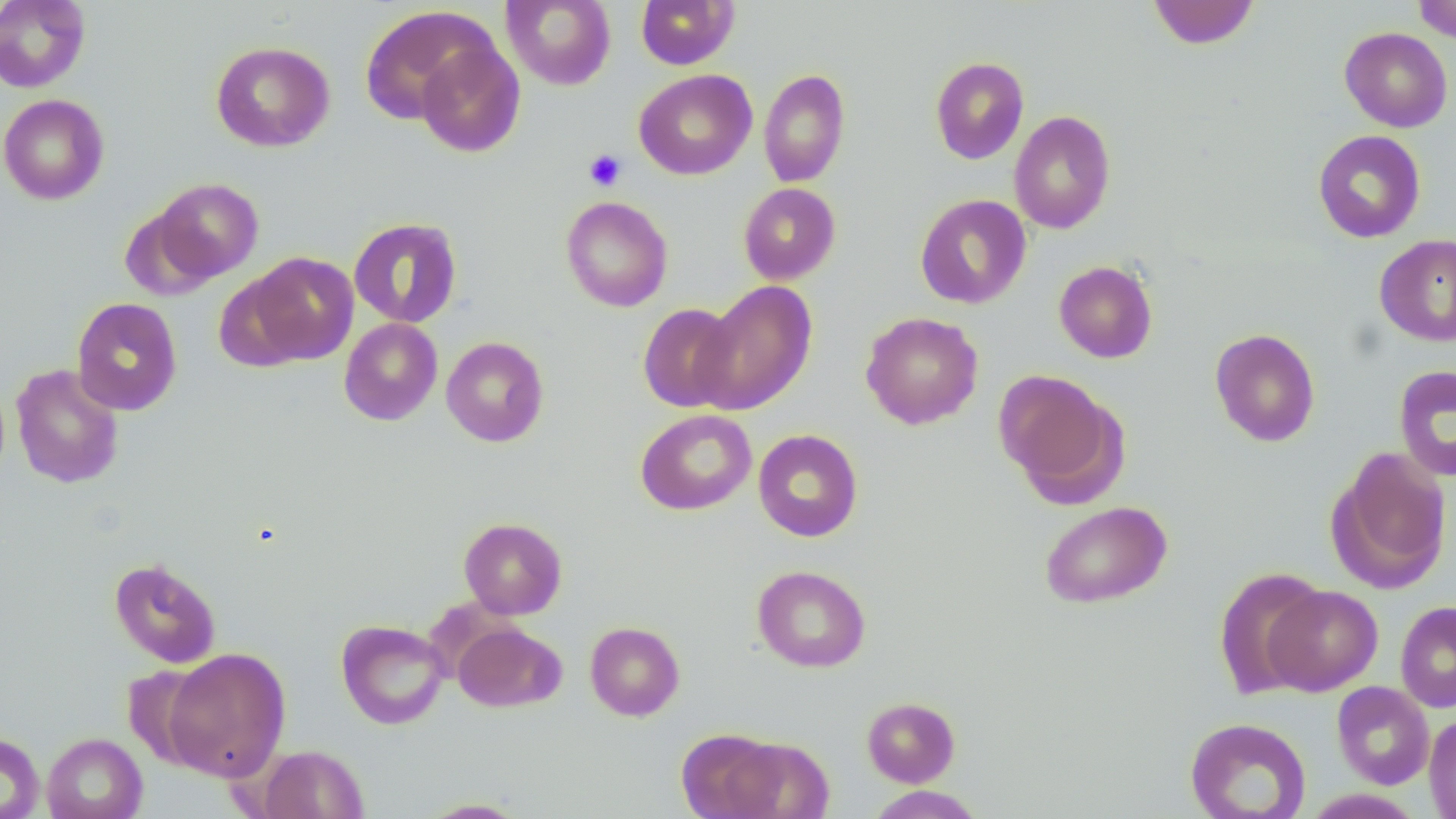
Approximate bounding boxes as (x1,y1)-(x2,y2) corner pairs in pixels. Uninfected red blood cell locations: (0,0)-(91,93), (501,0)-(616,90), (636,0)-(738,69), (1147,0)-(1260,50), (1413,0)-(1456,42), (359,6)-(495,125), (1339,27)-(1453,132), (415,40)-(526,157), (210,41)-(335,152), (930,56)-(1029,164), (759,68)-(851,188), (634,69)-(757,180), (0,94)-(109,205), (1009,110)-(1116,234), (1312,129)-(1426,243), (152,177)-(263,281), (738,182)-(841,285), (915,194)-(1032,309), (561,195)-(673,312), (120,206)-(221,302), (348,217)-(463,328), (1373,233)-(1456,347), (248,251)-(359,364), (1053,260)-(1158,363), (213,272)-(311,373), (695,281)-(818,415), (71,297)-(183,416), (638,303)-(741,412), (860,312)-(983,430), (339,318)-(443,426), (1209,328)-(1321,447), (441,336)-(549,447), (10,364)-(125,489), (1393,364)-(1456,482), (994,370)-(1125,504), (635,409)-(756,515), (753,429)-(863,541), (1327,447)-(1453,594), (1039,501)-(1172,609), (459,517)-(567,620), (108,557)-(221,668), (752,564)-(871,672), (1214,568)-(1327,698), (1263,585)-(1383,695), (1395,601)-(1456,712), (336,619)-(449,729), (585,621)-(684,721), (453,622)-(566,712), (162,648)-(290,781), (1332,681)-(1434,789), (862,696)-(960,787), (1423,712)-(1456,819), (1185,717)-(1311,819), (676,728)-(785,818), (0,732)-(45,819), (41,732)-(147,819), (725,736)-(834,819), (256,744)-(368,818), (866,786)-(985,818), (415,798)-(532,818). Platelet locations: (584,149)-(626,191). Slide-level diagnosis: no evidence of blood parasites. Light microscopy. Image is 1456×819 pixels. May-Grünwald-Giemsa stain. Thin blood film. Single field of view. 1000x magnification.